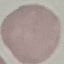

result = negative for malaria parasites
capture = smartphone camera at the microscope eyepiece
preparation = thin blood smear
image type = cell patch, automatically extracted from a larger field of view and resized to 64 × 64 pixels
stain = Giemsa